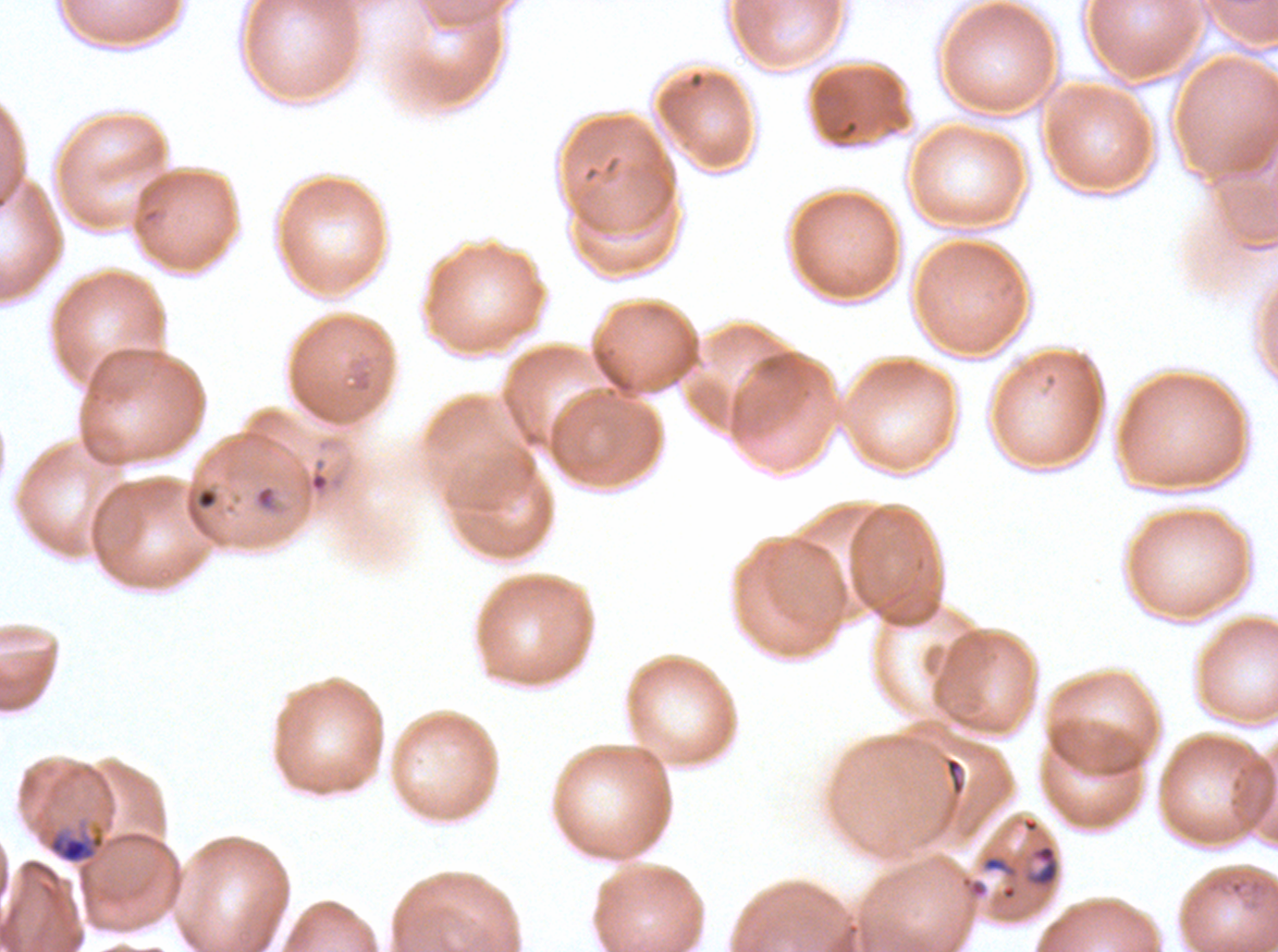

Approximate bounding rectangles given as corner coordinates in pixels from the top-left. Ring locations: (x1=194, y1=486, x2=220, y2=511), (x1=1025, y1=843, x2=1060, y2=889). Mid trophozoite locations: (x1=46, y1=830, x2=105, y2=865). Life-cycle stages observed: ring, mid trophozoite. Thin blood film. A sub-image separated from a larger composite. Ex-vivo Plasmodium falciparum culture from a patient in The Gambia, grown for 24 to 48 hours. Giemsa stain. Image is 1278×952 pixels.